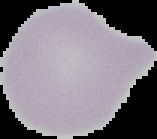

Image is 157×139 pixels. Result: no malaria parasites seen. The area outside the segmented cell region is set to black. From a thin blood film.